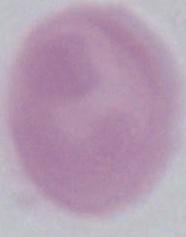

identification = red blood cell
modality = micrograph
magnification = 1000x